Outline each uninfected red blood cell.
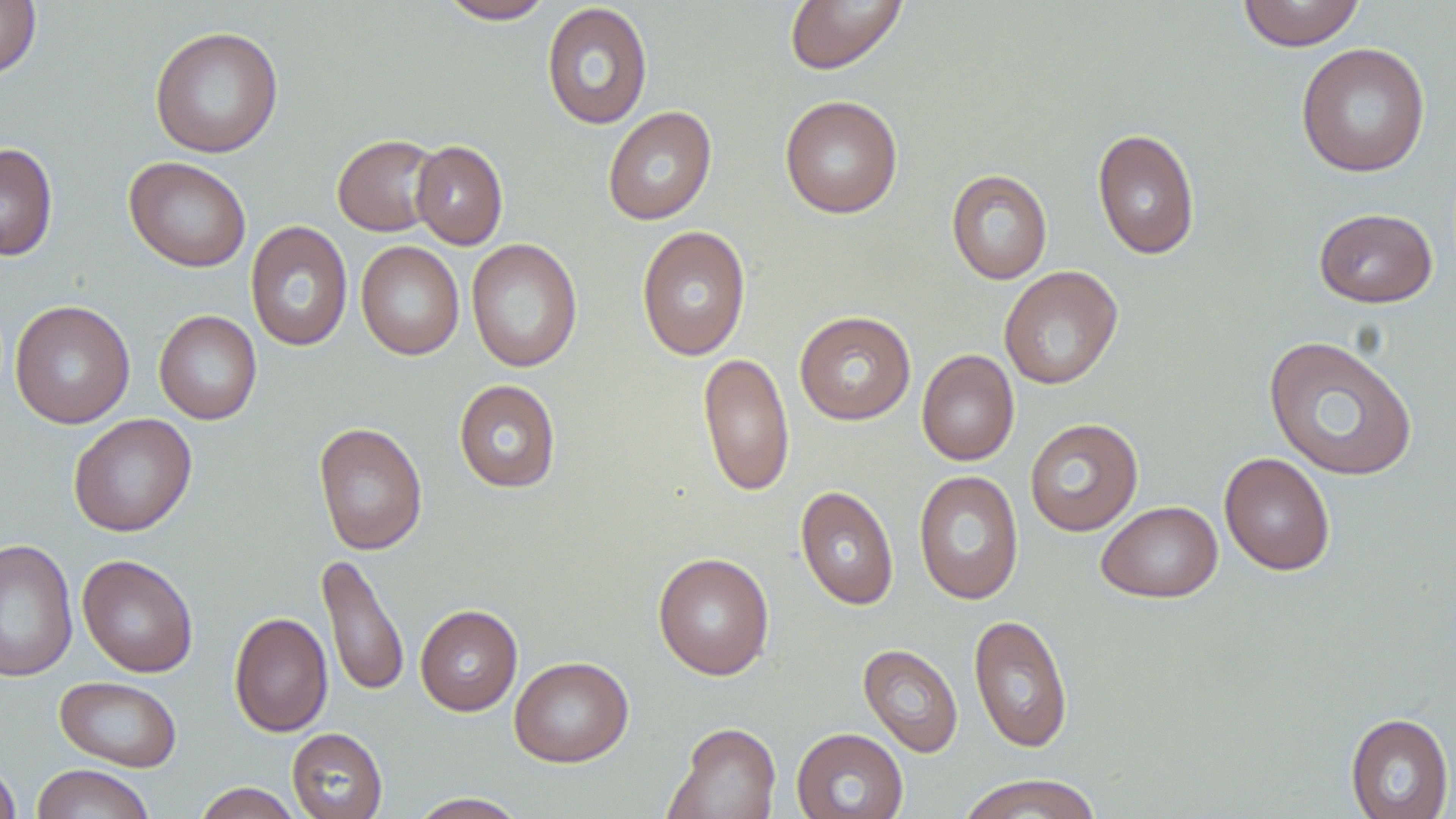
Approximate bounding boxes as (x1,y1)-(x2,y2) corner pairs in pixels.
Uninfected red blood cells: (0,0)-(41,79), (437,0)-(557,24), (784,0)-(908,74), (1236,0)-(1366,51), (541,3)-(653,130), (149,26)-(284,158), (1295,42)-(1431,178), (779,95)-(903,218), (602,106)-(717,225), (1092,127)-(1200,260), (333,134)-(442,236), (411,140)-(508,249), (0,142)-(58,261), (124,156)-(252,272), (947,169)-(1053,284), (1313,207)-(1438,308), (245,220)-(353,352), (636,225)-(752,361), (465,239)-(583,372), (355,241)-(465,360), (998,266)-(1123,390), (10,300)-(135,428), (153,310)-(262,425), (794,311)-(916,425), (1263,334)-(1419,482), (916,349)-(1019,466), (698,352)-(795,497), (454,379)-(561,493), (68,413)-(197,537), (1024,418)-(1143,536), (313,422)-(428,556), (1219,452)-(1335,576), (913,470)-(1025,606), (795,486)-(899,610), (1096,500)-(1223,603), (0,539)-(78,682), (653,552)-(775,680), (316,553)-(410,699), (77,554)-(198,677), (415,604)-(522,716), (229,611)-(332,738), (968,613)-(1073,753), (858,643)-(963,758), (509,655)-(634,767), (54,676)-(182,772), (1345,713)-(1454,819), (664,722)-(780,819), (792,727)-(908,819), (287,728)-(387,819), (0,761)-(21,819), (31,764)-(155,819), (957,774)-(1106,819), (192,782)-(304,818), (407,792)-(529,818).

slide-level diagnosis = negative for blood parasites
preparation = thin blood smear
magnification = 1000x
image size = 1456×819 pixels
stain = May-Grünwald-Giemsa
field of view = one of a larger specimen
modality = light microscopy